Point out each leukocyte.
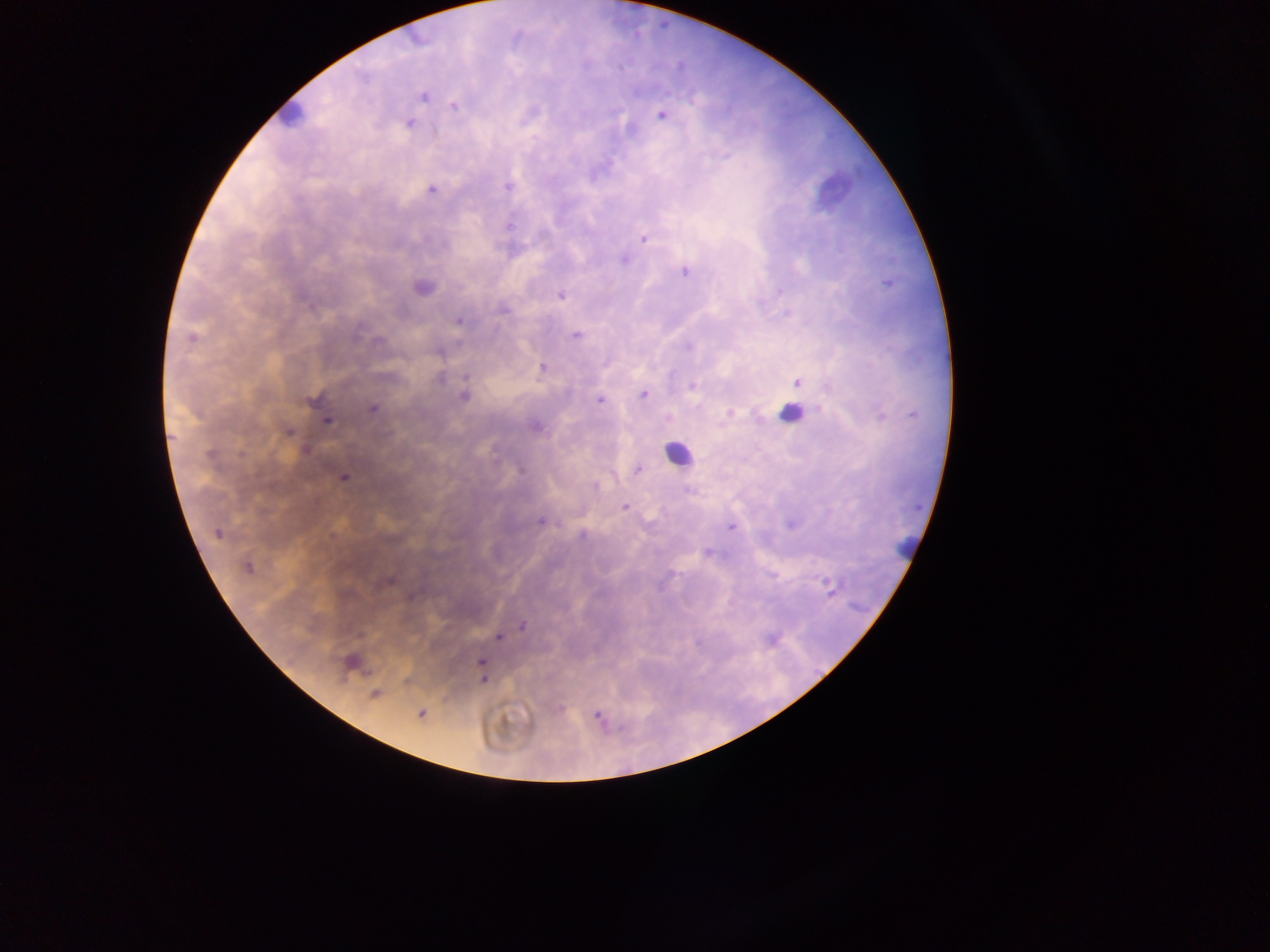
Approximate centers as x y in pixels.
Leukocytes: 289 115; 789 413; 678 454; 909 548.

Plasmodium parasite locations = approximate centers as x y in pixels: 423 96; 454 106; 661 114; 409 122; 508 186; 431 188; 644 237; 624 259; 685 271; 422 288; 561 295; 504 308; 459 321; 576 334; 192 338; 543 367; 797 382; 693 385; 643 394; 463 396; 599 399; 313 400; 372 408; 730 413; 326 419; 535 427; 286 432; 305 449; 637 470; 343 477; 625 506; 541 520; 731 528; 217 532; 708 552; 247 566; 387 581; 831 589; 522 626; 499 636; 352 662; 481 662; 483 678; 375 694; 420 713; 598 716
image size = 1270×952 pixels
capture = mobile-phone photograph through a microscope
preparation = thick blood film
country = Ghana
field of view = single